Classify this cell by malaria status.
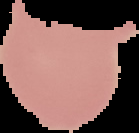
Uninfected.

Summary:
  - Image size: 139×133 pixels
  - Image type: cell region segmented out of the field of view; surrounding area masked to black
  - Preparation: thin blood smear